Classify this cell by malaria status.
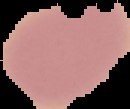
It is uninfected.

Summary:
  - Image type: cell region segmented out of the field of view; surrounding area masked to black
  - Preparation: thin blood film
  - Image size: 130×109 pixels